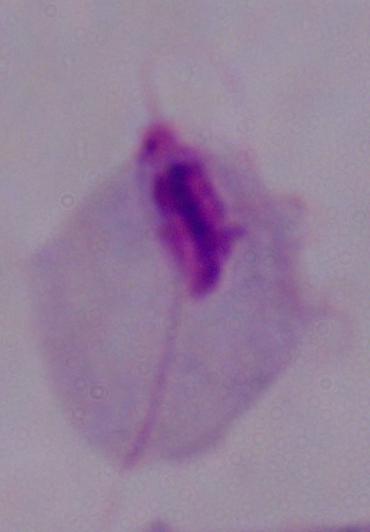 A trichomonad is shown. 1000x magnification. Micrograph.